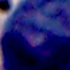
identification: leukocyte
modality: photomicrograph
magnification: 1000x